Name the blood parasite species.
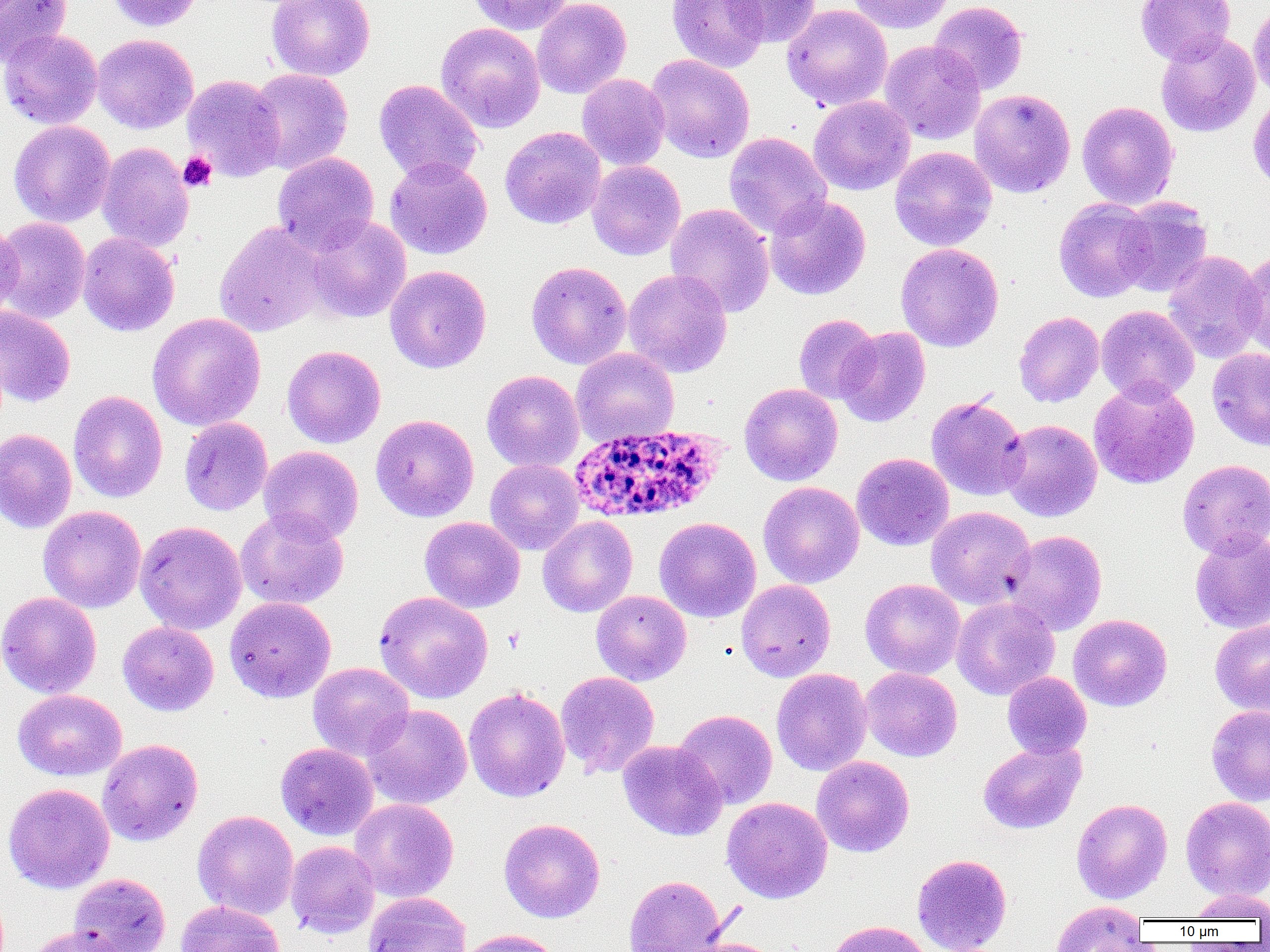
Plasmodium ovale.

Summary:
  - Coordinate format: approximate bounding boxes as named x1/y1/x2/y2 corners in pixels
  - Uninfected red blood cell locations: (x1=0, y1=0, x2=72, y2=65), (x1=105, y1=0, x2=203, y2=32), (x1=266, y1=0, x2=375, y2=81), (x1=468, y1=0, x2=574, y2=35), (x1=531, y1=0, x2=631, y2=99), (x1=667, y1=0, x2=770, y2=73), (x1=722, y1=0, x2=821, y2=47), (x1=846, y1=0, x2=954, y2=33), (x1=1135, y1=0, x2=1236, y2=65), (x1=929, y1=1, x2=1028, y2=95), (x1=1249, y1=1, x2=1270, y2=100), (x1=781, y1=4, x2=893, y2=111), (x1=435, y1=22, x2=545, y2=132), (x1=0, y1=29, x2=103, y2=129), (x1=1156, y1=30, x2=1260, y2=138), (x1=92, y1=34, x2=198, y2=134), (x1=880, y1=40, x2=986, y2=144), (x1=645, y1=54, x2=755, y2=163), (x1=248, y1=68, x2=353, y2=174), (x1=577, y1=73, x2=670, y2=170), (x1=181, y1=74, x2=285, y2=182), (x1=374, y1=79, x2=484, y2=185), (x1=969, y1=89, x2=1075, y2=198), (x1=1248, y1=94, x2=1270, y2=196), (x1=808, y1=95, x2=914, y2=195), (x1=1077, y1=100, x2=1178, y2=209), (x1=9, y1=120, x2=115, y2=227), (x1=500, y1=126, x2=606, y2=229), (x1=724, y1=132, x2=831, y2=238), (x1=97, y1=142, x2=195, y2=252), (x1=890, y1=146, x2=997, y2=250), (x1=272, y1=152, x2=379, y2=253), (x1=385, y1=157, x2=492, y2=259), (x1=587, y1=160, x2=686, y2=260), (x1=764, y1=194, x2=871, y2=300), (x1=1115, y1=196, x2=1213, y2=297), (x1=1053, y1=197, x2=1156, y2=302), (x1=665, y1=203, x2=775, y2=317), (x1=305, y1=215, x2=411, y2=323), (x1=0, y1=216, x2=91, y2=324), (x1=0, y1=220, x2=24, y2=323), (x1=214, y1=221, x2=329, y2=336), (x1=78, y1=231, x2=180, y2=337), (x1=895, y1=243, x2=1004, y2=352), (x1=1237, y1=247, x2=1270, y2=358), (x1=1163, y1=250, x2=1266, y2=363), (x1=526, y1=261, x2=632, y2=370), (x1=385, y1=265, x2=491, y2=373), (x1=623, y1=269, x2=733, y2=377), (x1=1096, y1=305, x2=1199, y2=405), (x1=0, y1=306, x2=76, y2=407), (x1=1014, y1=311, x2=1104, y2=407), (x1=146, y1=313, x2=266, y2=431), (x1=793, y1=314, x2=879, y2=404), (x1=835, y1=326, x2=931, y2=427), (x1=282, y1=345, x2=386, y2=448), (x1=571, y1=348, x2=679, y2=446), (x1=1207, y1=348, x2=1270, y2=451), (x1=481, y1=369, x2=584, y2=472), (x1=1088, y1=379, x2=1200, y2=489), (x1=739, y1=383, x2=842, y2=486), (x1=68, y1=390, x2=168, y2=503), (x1=926, y1=395, x2=1029, y2=501), (x1=370, y1=414, x2=479, y2=522), (x1=179, y1=417, x2=273, y2=516), (x1=1000, y1=419, x2=1102, y2=521), (x1=0, y1=428, x2=77, y2=534), (x1=258, y1=446, x2=364, y2=544), (x1=851, y1=452, x2=954, y2=551), (x1=485, y1=459, x2=584, y2=555), (x1=1177, y1=459, x2=1270, y2=558), (x1=757, y1=481, x2=864, y2=588), (x1=38, y1=506, x2=146, y2=613), (x1=926, y1=506, x2=1036, y2=609), (x1=235, y1=508, x2=349, y2=609), (x1=537, y1=515, x2=638, y2=617), (x1=419, y1=516, x2=525, y2=613), (x1=654, y1=517, x2=761, y2=622), (x1=135, y1=521, x2=247, y2=635), (x1=1005, y1=530, x2=1108, y2=635), (x1=1190, y1=530, x2=1270, y2=633), (x1=860, y1=578, x2=965, y2=679), (x1=736, y1=579, x2=836, y2=682), (x1=373, y1=590, x2=493, y2=703), (x1=591, y1=590, x2=691, y2=685), (x1=0, y1=591, x2=101, y2=698), (x1=225, y1=596, x2=336, y2=703), (x1=951, y1=597, x2=1059, y2=700), (x1=1068, y1=614, x2=1172, y2=712), (x1=1210, y1=620, x2=1270, y2=717), (x1=117, y1=621, x2=219, y2=716), (x1=308, y1=662, x2=414, y2=760), (x1=861, y1=667, x2=962, y2=762), (x1=772, y1=668, x2=872, y2=775), (x1=555, y1=671, x2=660, y2=778), (x1=1002, y1=672, x2=1091, y2=759), (x1=464, y1=686, x2=570, y2=802), (x1=12, y1=689, x2=127, y2=781), (x1=361, y1=704, x2=472, y2=809), (x1=1207, y1=704, x2=1270, y2=806), (x1=674, y1=709, x2=777, y2=809), (x1=97, y1=739, x2=203, y2=847), (x1=978, y1=739, x2=1086, y2=834), (x1=617, y1=740, x2=726, y2=840), (x1=276, y1=742, x2=378, y2=840), (x1=812, y1=756, x2=914, y2=857), (x1=3, y1=783, x2=115, y2=893), (x1=1181, y1=796, x2=1270, y2=900), (x1=722, y1=797, x2=832, y2=903), (x1=349, y1=798, x2=459, y2=902), (x1=1072, y1=798, x2=1172, y2=903), (x1=193, y1=810, x2=298, y2=919), (x1=498, y1=818, x2=605, y2=923), (x1=285, y1=841, x2=379, y2=938), (x1=912, y1=853, x2=1012, y2=952), (x1=68, y1=873, x2=171, y2=952), (x1=624, y1=875, x2=725, y2=951), (x1=1187, y1=889, x2=1270, y2=921), (x1=363, y1=892, x2=472, y2=952), (x1=176, y1=900, x2=284, y2=952), (x1=1051, y1=900, x2=1148, y2=952), (x1=825, y1=920, x2=933, y2=952), (x1=25, y1=926, x2=131, y2=952), (x1=456, y1=929, x2=563, y2=952), (x1=681, y1=938, x2=786, y2=952)
  - Plasmodium ovale-infected red blood cell locations: (x1=567, y1=423, x2=726, y2=525)
  - Platelet locations: (x1=178, y1=151, x2=217, y2=192)
  - Field of view: single
  - Image size: 1270×952 pixels
  - Preparation: thin blood film
  - Magnification: 1000x
  - Modality: optical microscopy